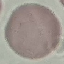

Result: no malaria parasites detected. Photographed with a smartphone camera at the microscope eyepiece. Giemsa stain. Automatically extracted cell patch, resized to 64 × 64 pixels. Thin blood smear.